Classify this cell by malaria status.
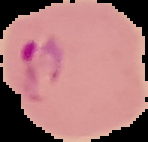

It is parasitized.

preparation = thin blood smear
image size = 148×142 pixels
image type = cell region segmented out of the field of view; surrounding area masked to black